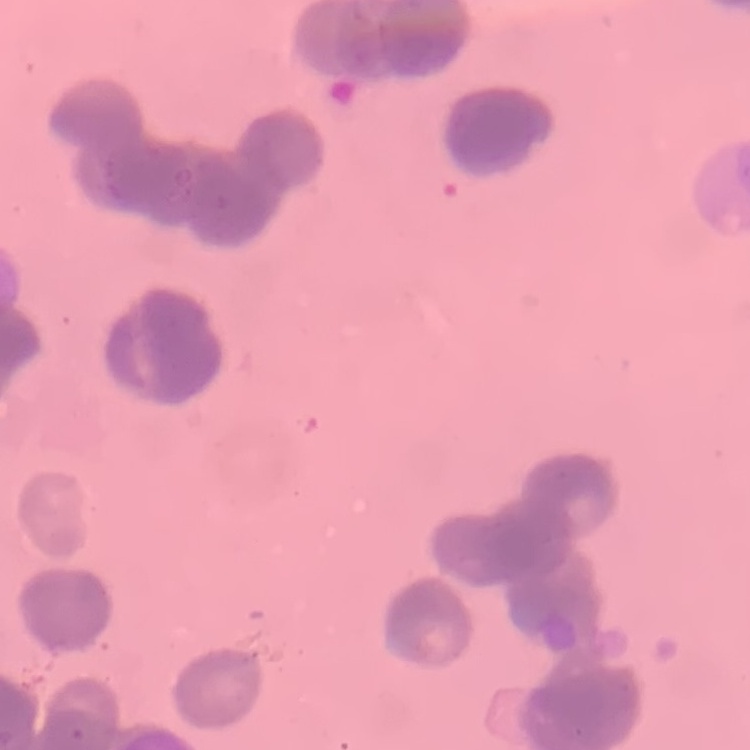

red blood cell morphology = rouleaux formation
image type = square crop of a larger photomicrograph
stain = Field's or Giemsa
preparation = thin blood smear